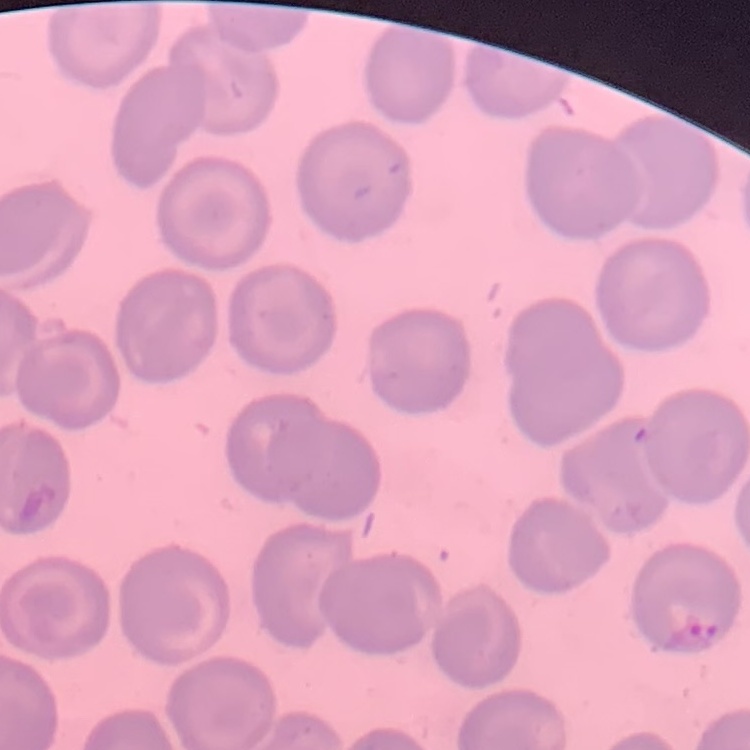

{
  "erythrocyte_morphology": "no rouleaux formation",
  "stain": "Field's or Giemsa",
  "preparation": "thin blood smear",
  "image_type": "one tile cut from a larger photomicrograph"
}